State which cell type is depicted.
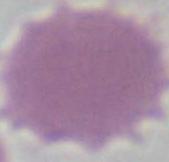
This is an erythrocyte.

Summary:
  - Modality: photomicrograph
  - Magnification: 1000x